Outline each blood parasite and name the species.
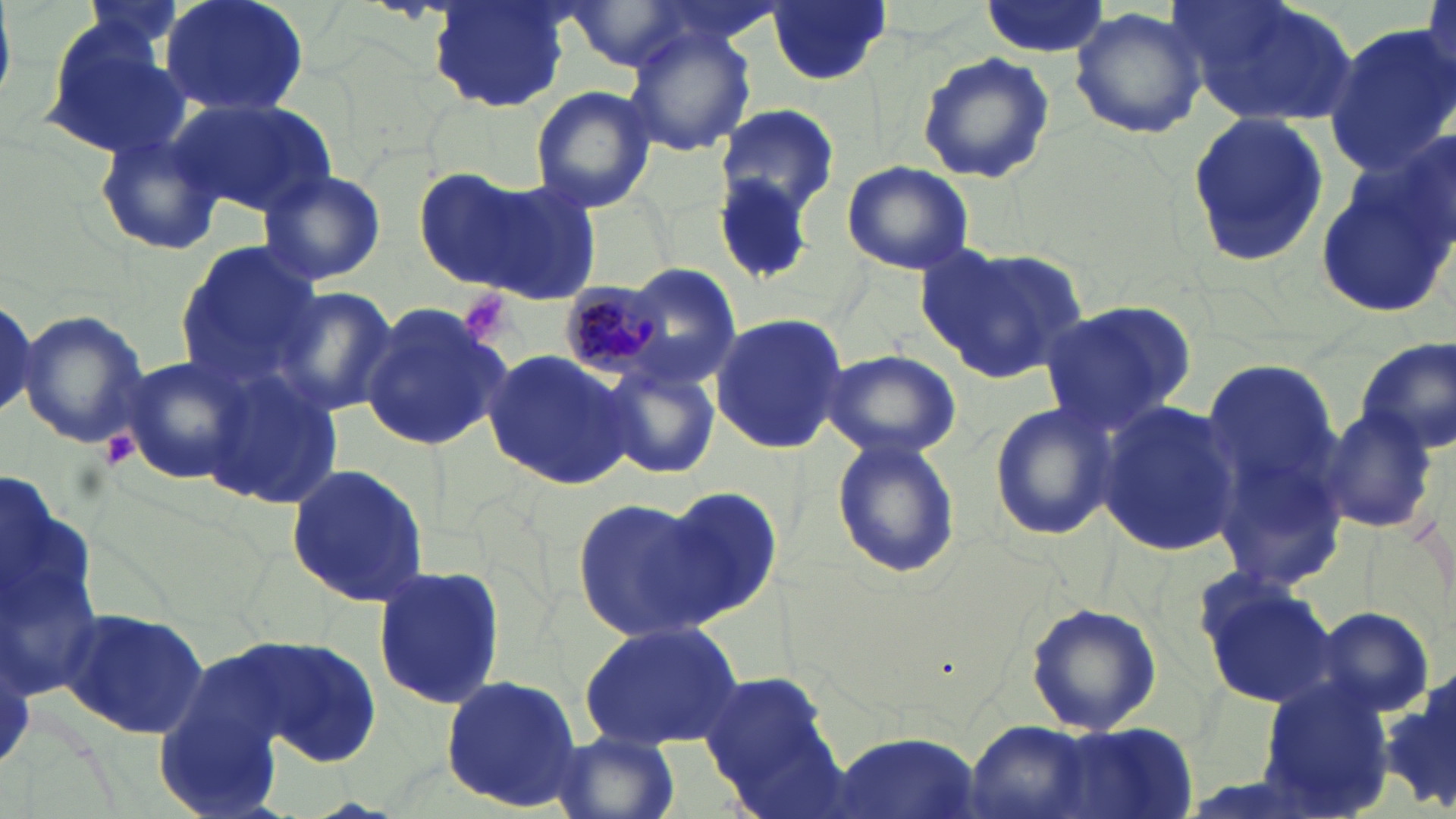
Approximate bounding boxes as [x1, y1, x2, y2] in pixels.
Plasmodium malariae-infected red blood cells: [558, 279, 665, 379].
No Plasmodium falciparum, Plasmodium ovale, Plasmodium vivax, Babesia divergens, or Trypanosoma brucei observed.

Summary:
  - Platelet locations: [456, 288, 514, 344], [99, 433, 140, 470]
  - Uninfected red blood cell locations: [159, 0, 310, 117], [980, 0, 1111, 58], [1173, 0, 1362, 127], [430, 1, 571, 112], [768, 1, 891, 86], [564, 2, 696, 72], [1068, 7, 1210, 141], [624, 24, 758, 156], [1322, 24, 1456, 179], [39, 25, 189, 157], [915, 51, 1056, 184], [529, 85, 658, 214], [172, 97, 333, 217], [715, 105, 839, 216], [1185, 112, 1328, 265], [93, 123, 227, 258], [1315, 155, 1456, 318], [841, 159, 975, 276], [409, 164, 565, 292], [257, 167, 387, 287], [464, 173, 605, 306], [173, 240, 323, 392], [916, 241, 1092, 382], [619, 263, 743, 390], [269, 284, 399, 418], [0, 288, 57, 431], [1039, 300, 1195, 435], [357, 303, 513, 454], [18, 309, 149, 449], [709, 312, 849, 454], [1357, 337, 1456, 457], [482, 347, 640, 491], [822, 350, 961, 459], [116, 356, 253, 486], [1198, 362, 1343, 507], [604, 365, 721, 477], [203, 368, 342, 511], [987, 400, 1117, 543], [1095, 400, 1244, 555], [1317, 407, 1441, 537], [1205, 412, 1353, 598], [830, 437, 963, 579], [282, 464, 435, 609], [657, 487, 784, 623], [571, 495, 719, 644], [373, 565, 508, 712], [1193, 572, 1340, 710], [1024, 601, 1160, 734], [59, 605, 211, 740], [1311, 606, 1436, 717], [580, 622, 745, 752], [250, 637, 383, 766], [697, 665, 846, 812], [440, 672, 587, 813], [1383, 673, 1456, 816], [1255, 677, 1396, 814], [1004, 720, 1204, 816], [964, 721, 1101, 819], [827, 731, 978, 819], [551, 732, 679, 819]
  - White blood cell locations: [0, 450, 98, 730]
  - Slide-level diagnosis: Plasmodium malariae
  - Stain: May-Grünwald-Giemsa
  - Modality: optical microscopy
  - Field of view: single
  - Magnification: 1000x
  - Image size: 1456×819 pixels
  - Preparation: thin blood film